Outline white blood cells.
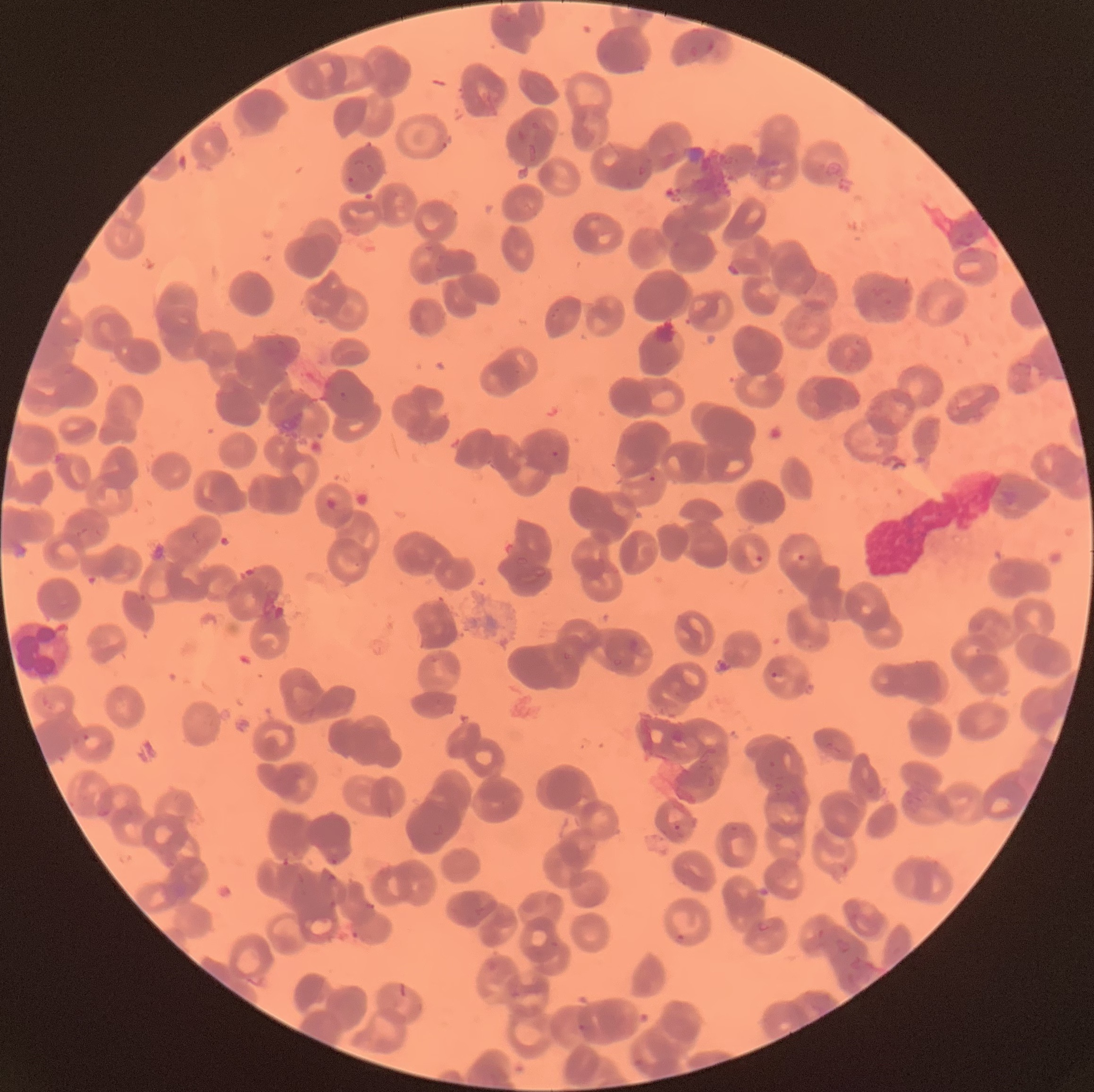
Approximate bounding boxes as (x1,y1)-(x2,y2) corner pairs in pixels.
White blood cells: (12,622)-(74,681).

{
  "plasmodium_parasite_locations": "approximate bounding boxes as (x1,y1)-(x2,y2) corner pairs in pixels: (346,176)-(355,186), (550,451)-(559,457), (326,497)-(339,512), (797,552)-(805,563), (756,554)-(764,564), (769,672)-(778,679), (82,734)-(102,752), (673,824)-(681,831), (328,858)-(340,866), (350,931)-(360,939), (676,933)-(687,945), (577,1024)-(589,1032), (635,1058)-(644,1068)",
  "plasmodium_parasites_too_small_for_a_box": "approximate centers as (x,y) in pixels: (652,478)",
  "red_blood_cell_morphology": "rouleaux formation",
  "image_size": "1094×1092 pixels",
  "preparation": "thin blood smear",
  "modality": "optical microscopy"
}